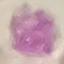
result = negative for malaria parasites
capture = smartphone through the microscope eyepiece
stain = Giemsa
preparation = thin blood film
image type = automatically extracted cell patch, resized to 64 × 64 pixels